Assess this cell for malaria.
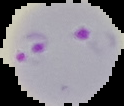
It is parasitized.

Summary:
  - Preparation: thin blood smear
  - Image size: 124×106 pixels
  - Image type: segmented cell region on a black background